Assess this cell for malaria.
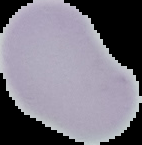
Uninfected.

Summary:
  - Image size: 142×145 pixels
  - Image type: segmented cell region with the area outside set to black
  - Preparation: thin blood film